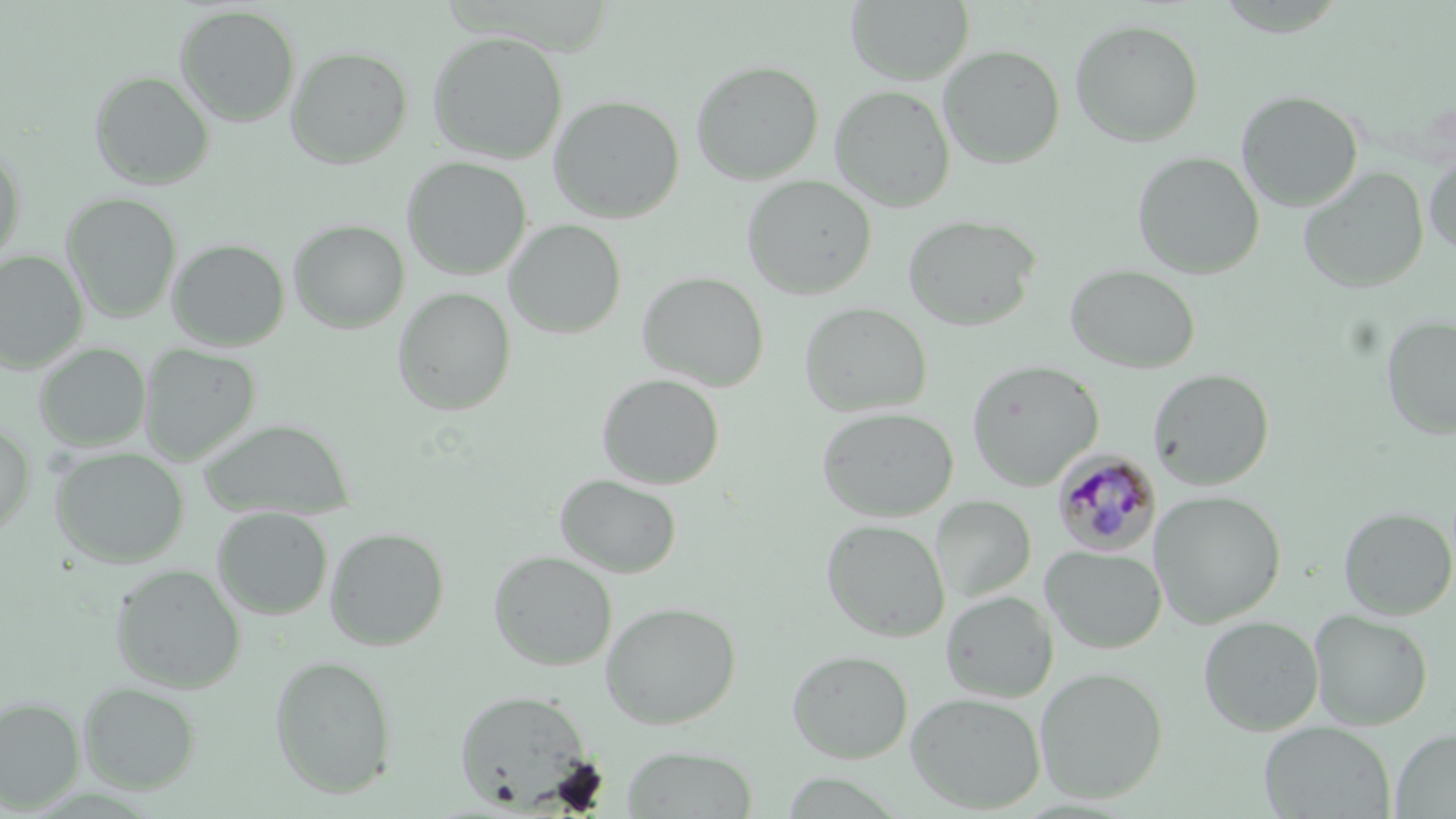
slide_level_diagnosis: Plasmodium malariae
field_of_view: one of a larger specimen
magnification: 1000x
image_size: 1456×819 pixels
plasmodium_malariae_infected_red_blood_cell_locations: 'approximate bounding boxes as (x1,y1)-(x2,y2) corner pairs in pixels: (1053,450)-(1162,558)'
preparation: thin blood film
uninfected_red_blood_cell_locations: 'approximate bounding boxes as (x1,y1)-(x2,y2) corner pairs in pixels: (846,0)-(974,85), (174,5)-(301,127), (1070,18)-(1205,147), (426,30)-(568,164), (938,44)-(1066,169), (285,45)-(413,170), (690,59)-(824,185), (88,71)-(215,190), (829,85)-(955,211), (1235,90)-(1363,212), (548,94)-(685,224), (0,147)-(26,269), (1424,150)-(1456,257), (1131,151)-(1265,279), (401,156)-(532,281), (1299,166)-(1429,294), (741,175)-(877,300), (60,193)-(183,323), (902,213)-(1041,331), (287,219)-(410,334), (503,219)-(627,339), (167,238)-(290,351), (0,250)-(88,373), (1065,263)-(1201,373), (637,271)-(769,391), (392,287)-(516,416), (800,301)-(932,417), (1381,315)-(1456,440), (33,343)-(151,451), (40,343)-(169,555), (138,343)-(262,465), (965,359)-(1104,491), (1148,368)-(1275,490), (596,373)-(725,490), (817,406)-(959,523), (199,419)-(354,521), (0,423)-(35,538), (50,447)-(189,567), (554,473)-(682,579), (1150,490)-(1287,628), (931,495)-(1036,603), (212,506)-(333,620), (1338,506)-(1456,619), (821,518)-(950,642), (324,526)-(450,650), (1041,544)-(1167,654), (488,550)-(617,671), (110,563)-(246,693), (941,590)-(1058,703), (600,601)-(742,729), (1308,609)-(1433,730), (1198,615)-(1324,736), (786,648)-(914,763), (269,654)-(398,798), (1035,666)-(1169,803), (77,682)-(201,795), (454,689)-(594,810), (906,691)-(1046,814), (0,696)-(85,813), (1258,722)-(1395,818), (1391,728)-(1456,818), (621,745)-(758,818)'
stain: May-Grünwald-Giemsa
modality: optical microscopy